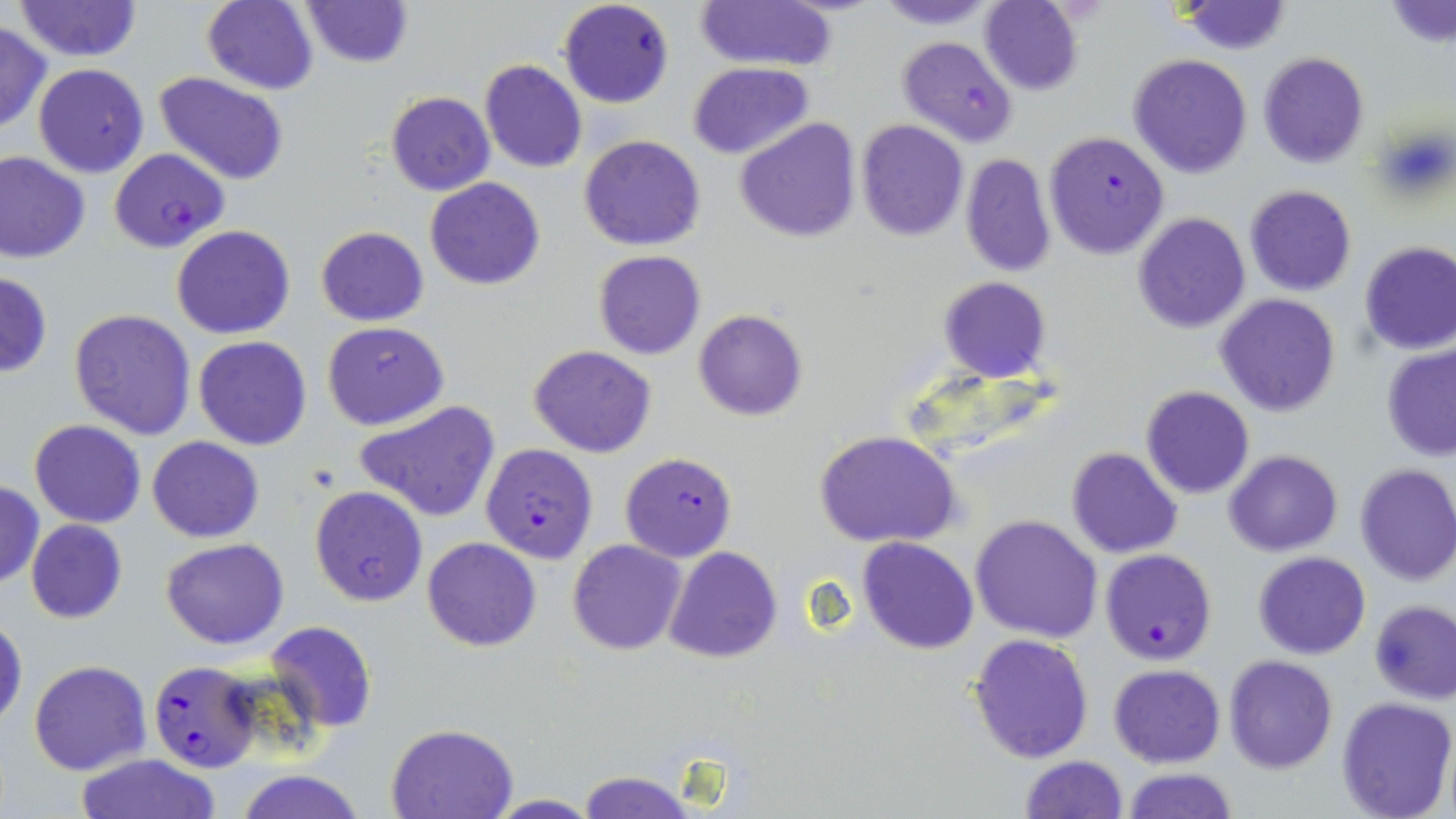 Approximate bounding boxes as [x1, y1, x2, y2] in pixels. Uninfected red blood cell locations: [13, 0, 144, 61], [202, 0, 319, 95], [694, 0, 839, 74], [869, 0, 1006, 29], [300, 1, 413, 68], [979, 1, 1085, 94], [1179, 1, 1291, 55], [1384, 2, 1456, 49], [0, 21, 50, 134], [1258, 52, 1370, 169], [1129, 53, 1253, 178], [479, 60, 588, 174], [688, 62, 812, 159], [33, 63, 148, 176], [153, 72, 292, 186], [386, 91, 494, 196], [736, 117, 859, 243], [857, 120, 969, 241], [579, 134, 705, 251], [0, 151, 91, 263], [959, 153, 1058, 276], [424, 177, 546, 290], [1243, 185, 1357, 297], [1133, 213, 1250, 333], [171, 224, 296, 339], [315, 225, 429, 327], [1359, 242, 1456, 355], [594, 251, 706, 360], [0, 270, 52, 378], [938, 277, 1051, 382], [1215, 293, 1341, 418], [68, 308, 196, 440], [693, 309, 808, 421], [322, 321, 449, 429], [192, 336, 313, 450], [1381, 344, 1456, 461], [528, 345, 656, 458], [1140, 385, 1254, 498], [356, 399, 501, 523], [29, 420, 146, 528], [816, 429, 962, 550], [146, 435, 265, 542], [1065, 447, 1184, 560], [1225, 450, 1343, 557], [1354, 463, 1456, 585], [0, 481, 44, 588], [310, 485, 428, 606], [971, 514, 1103, 643], [26, 518, 127, 622], [423, 537, 542, 652], [161, 538, 289, 650], [566, 538, 687, 656], [857, 538, 980, 656], [664, 546, 782, 664], [1251, 552, 1371, 659], [1369, 599, 1456, 704], [1, 614, 27, 730], [263, 619, 378, 733], [967, 633, 1095, 763], [1224, 655, 1338, 772], [29, 659, 151, 776], [1108, 663, 1226, 767], [1335, 696, 1456, 819], [386, 723, 518, 818], [73, 753, 222, 819], [1017, 754, 1129, 819], [1121, 767, 1237, 819], [232, 769, 366, 819], [578, 769, 694, 819], [486, 794, 600, 818]. Plasmodium falciparum-infected red blood cell locations: [557, 0, 674, 109], [897, 35, 1018, 149], [1044, 131, 1169, 258], [108, 148, 230, 252], [480, 443, 599, 564], [620, 451, 737, 562], [1099, 548, 1218, 665], [147, 660, 261, 774]. Slide-level diagnosis: Plasmodium falciparum. Image is 1456×819 pixels. Optical microscopy. One field of a larger specimen. Thin blood smear. May-Grünwald-Giemsa-stained preparation. 1000x magnification.